Classify the preparation.
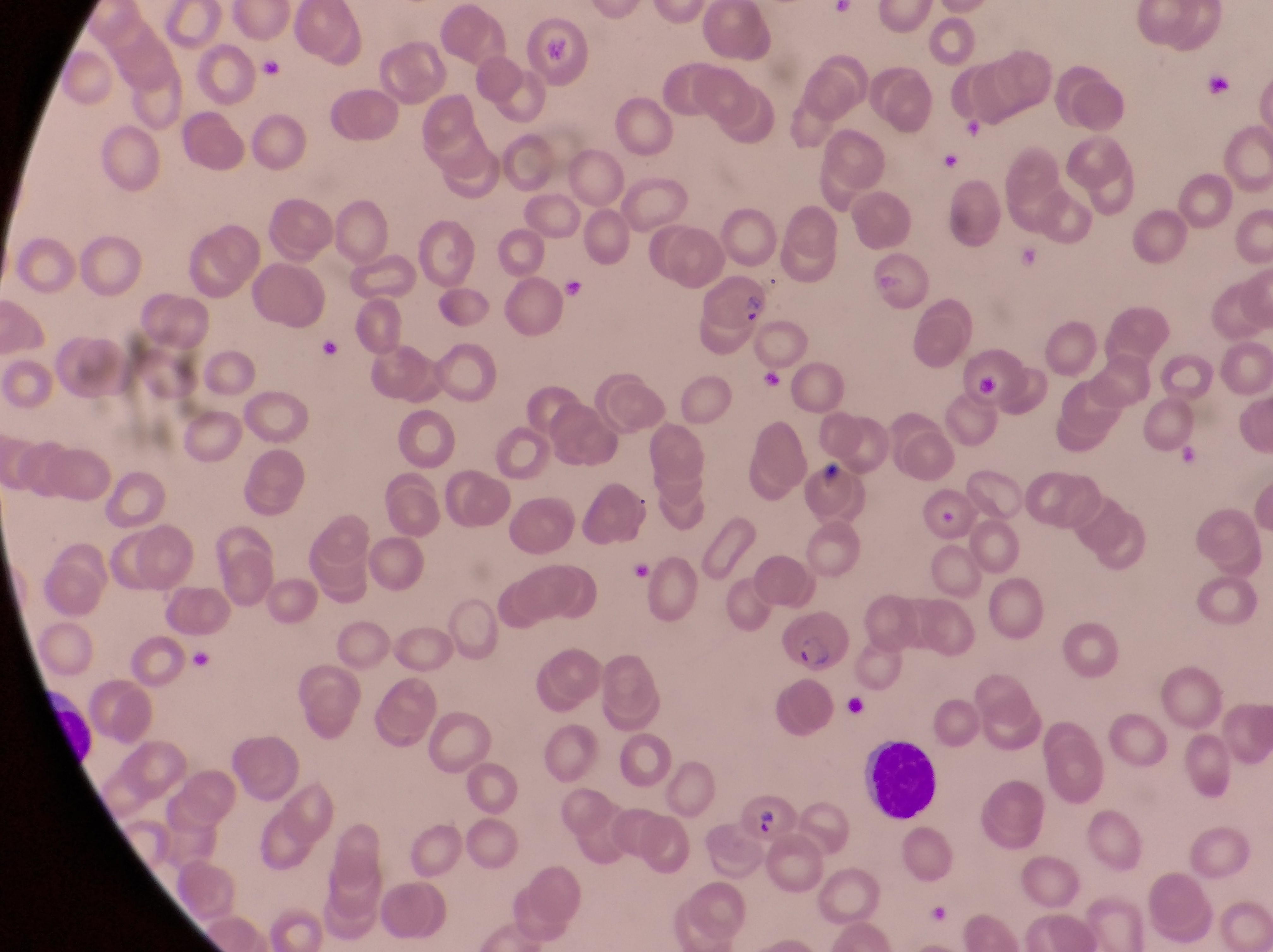
Thin blood smear.

magnification = 1000x
country = Uganda
field of view = single
trophozoite locations = approximate bounding boxes as [left, top, right, bottom] in pixels: [257, 53, 287, 86], [939, 148, 967, 176], [559, 272, 587, 307], [315, 334, 345, 369], [754, 357, 781, 394], [1169, 444, 1202, 472]
capture = smartphone photograph through the eyepiece of an Olympus CX-23 microscope
parasitised red blood cell locations = approximate bounding boxes as [left, top, right, bottom] in pixels: [517, 12, 592, 86], [859, 248, 931, 311], [699, 277, 771, 334], [808, 465, 865, 522], [921, 487, 978, 547], [778, 609, 856, 674], [739, 794, 801, 849]
image size = 1273×952 pixels
leukocyte locations = approximate bounding boxes as [left, top, right, bottom] in pixels: [858, 739, 940, 822]
artifact (platelet-like body, stain precipitate, or debris) locations = approximate bounding boxes as [left, top, right, bottom] in pixels: [1196, 74, 1236, 106], [966, 347, 1029, 414], [843, 691, 873, 719]